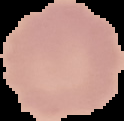

image size = 124×121 pixels
image type = segmented cell region on a black background
preparation = thin blood smear
malaria status = uninfected